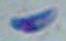

Summary:
  - Magnification: 1000x
  - Identification: Toxoplasma gondii
  - Modality: micrograph